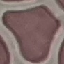

Result: no malaria parasites detected. Cell patch, automatically extracted from a larger field of view and resized to 64 × 64 pixels. Giemsa stain. Acquired by smartphone through the microscope eyepiece. Thin blood smear.